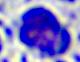
Summary:
  - Modality: micrograph
  - Identification: leukocyte
  - Magnification: 400x